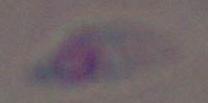
Captured at 1000x magnification. Toxoplasma gondii is seen. Photomicrograph.